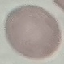

Malaria status: uninfected. Thin blood smear. Automatically extracted cell patch, resized to 64 × 64 pixels. Giemsa stain. Photographed with a smartphone camera at the microscope eyepiece.